Classify this cell by malaria status.
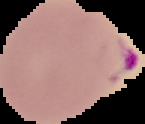
Parasitized.

{
  "image_type": "segmented cell region on a black background",
  "image_size": "145×124 pixels",
  "preparation": "thin blood film"
}